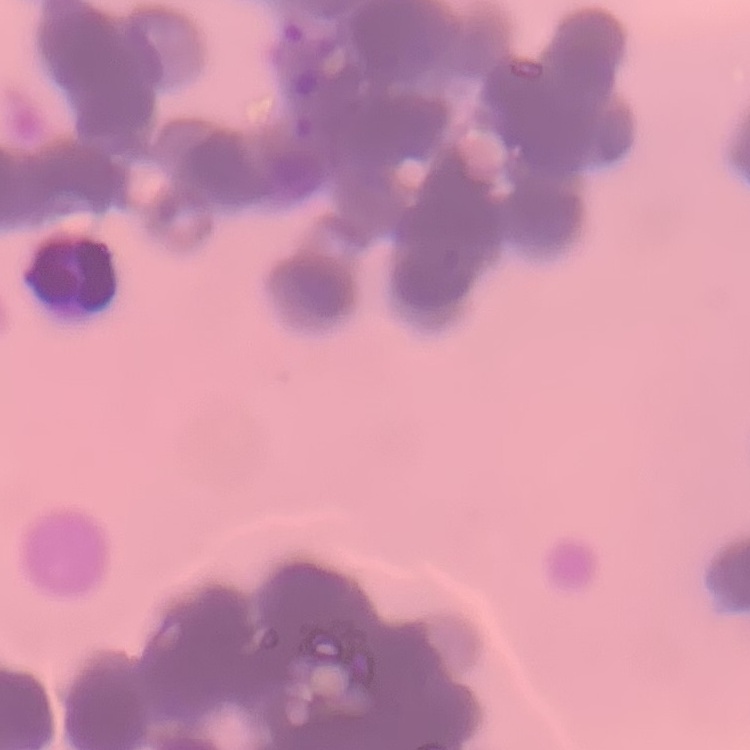

The erythrocytes show rouleaux formation. One tile cut from a larger photomicrograph. Stained with either Field's or Giemsa. Thin peripheral smear.